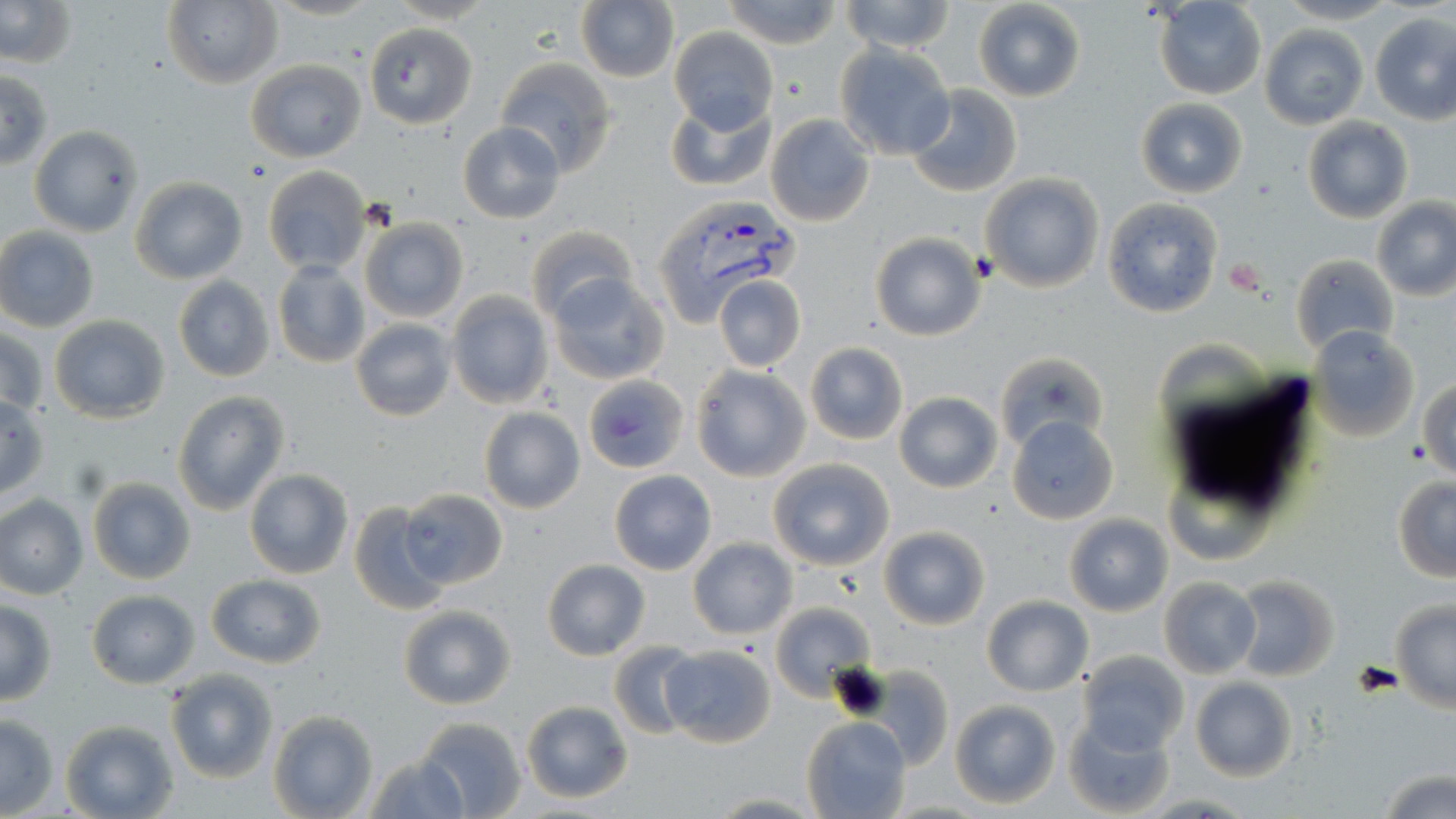

Summary:
  - Coordinate format: approximate bounding boxes as (x1,y1)-(x2,y2) corner pairs in pixels
  - Uninfected red blood cell locations: (0,0)-(77,68), (576,0)-(680,84), (721,0)-(842,48), (838,0)-(958,53), (1276,0)-(1399,25), (161,1)-(282,88), (974,1)-(1086,102), (1154,1)-(1267,100), (1368,12)-(1455,124), (364,22)-(477,129), (1260,25)-(1369,130), (668,28)-(779,134), (835,44)-(956,160), (494,57)-(619,175), (245,59)-(366,163), (0,71)-(53,170), (906,85)-(1021,198), (665,94)-(777,193), (1135,98)-(1248,198), (765,114)-(875,228), (1302,117)-(1413,223), (458,122)-(565,223), (29,126)-(143,237), (262,164)-(372,276), (979,173)-(1104,293), (130,178)-(248,285), (1101,196)-(1225,320), (1371,197)-(1456,301), (360,217)-(469,323), (524,225)-(636,325), (1,226)-(100,333), (870,232)-(987,342), (1290,254)-(1398,356), (272,260)-(371,368), (547,273)-(670,385), (713,274)-(807,373), (173,277)-(275,382), (445,292)-(552,410), (49,315)-(170,422), (350,318)-(457,422), (1309,326)-(1420,444), (1,327)-(49,419), (805,343)-(907,445), (993,351)-(1109,454), (691,365)-(809,482), (586,373)-(681,476), (1419,377)-(1455,479), (173,390)-(288,514), (895,391)-(1003,493), (0,396)-(50,502), (479,408)-(584,513), (1007,416)-(1119,524), (767,458)-(895,571), (1164,468)-(1275,565), (244,469)-(354,579), (609,470)-(717,575), (1392,474)-(1456,581), (86,476)-(197,585), (399,488)-(508,590), (0,495)-(87,599), (348,501)-(449,616), (1064,515)-(1172,616), (879,525)-(992,631), (687,539)-(796,638), (542,559)-(650,660), (205,573)-(327,668), (1232,575)-(1340,681), (1158,578)-(1261,678), (85,590)-(200,689), (982,595)-(1092,696), (0,600)-(56,705), (769,601)-(875,700), (1390,603)-(1456,712), (398,604)-(518,711), (609,640)-(700,738), (659,645)-(777,748), (1077,650)-(1190,755), (166,668)-(278,783), (866,668)-(951,768), (1190,677)-(1298,781), (949,699)-(1061,809), (519,700)-(634,803), (267,710)-(378,819), (1064,710)-(1178,818), (0,711)-(59,815), (802,716)-(912,819), (412,717)-(527,819), (59,719)-(179,819), (362,752)-(472,819), (1378,765)-(1456,819), (702,792)-(826,817), (1140,794)-(1256,816)
  - Plasmodium vivax-infected red blood cell locations: (650,199)-(798,325)
  - Slide-level diagnosis: Plasmodium vivax
  - Stain: May-Grünwald-Giemsa
  - Preparation: thin blood film
  - Magnification: 1000x
  - Field of view: single
  - Modality: light microscopy
  - Image size: 1456×819 pixels